Comment on the morphology of the erythrocytes.
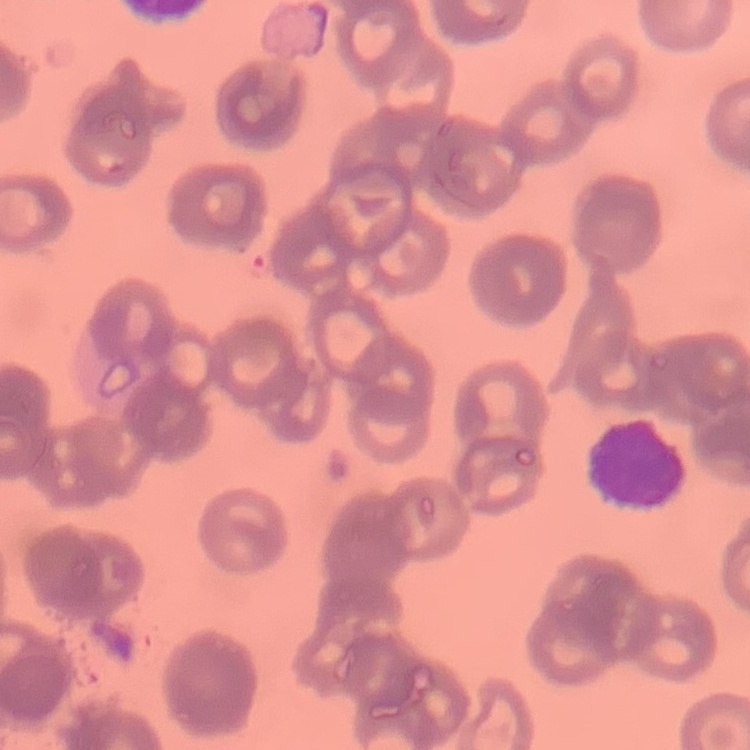
Rouleaux formation.

Summary:
  - Image type: one tile cut from a larger photomicrograph
  - Preparation: thin blood smear
  - Stain: Field's or Giemsa